Classify this cell by malaria status.
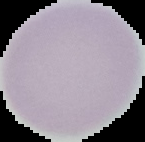

Uninfected.

Segmented cell region on a black background. From a thin blood smear. Image is 145×142 pixels.